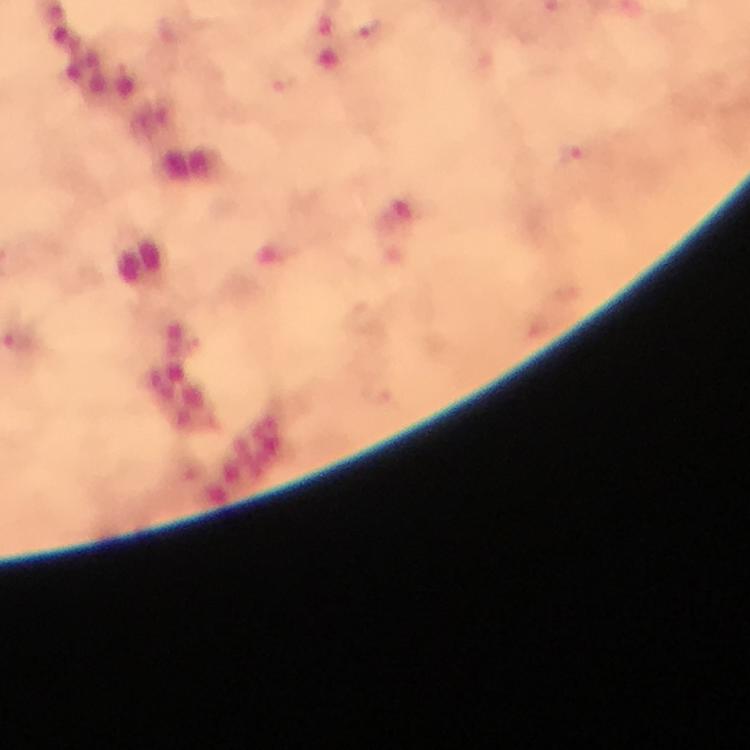

Approximate centers as {x, y} in pixels. Plasmodium parasite locations: {371, 33}, {280, 80}, {574, 153}. Photographed through the microscope with a smartphone camera. Giemsa-stained preparation. Image is 750×750 pixels. Cropped region of a single field of view. Thick smear. From a malaria diagnostic workup. Immersion oil was used. 100x magnification.